Give the extent of all Trypanosoma brucei.
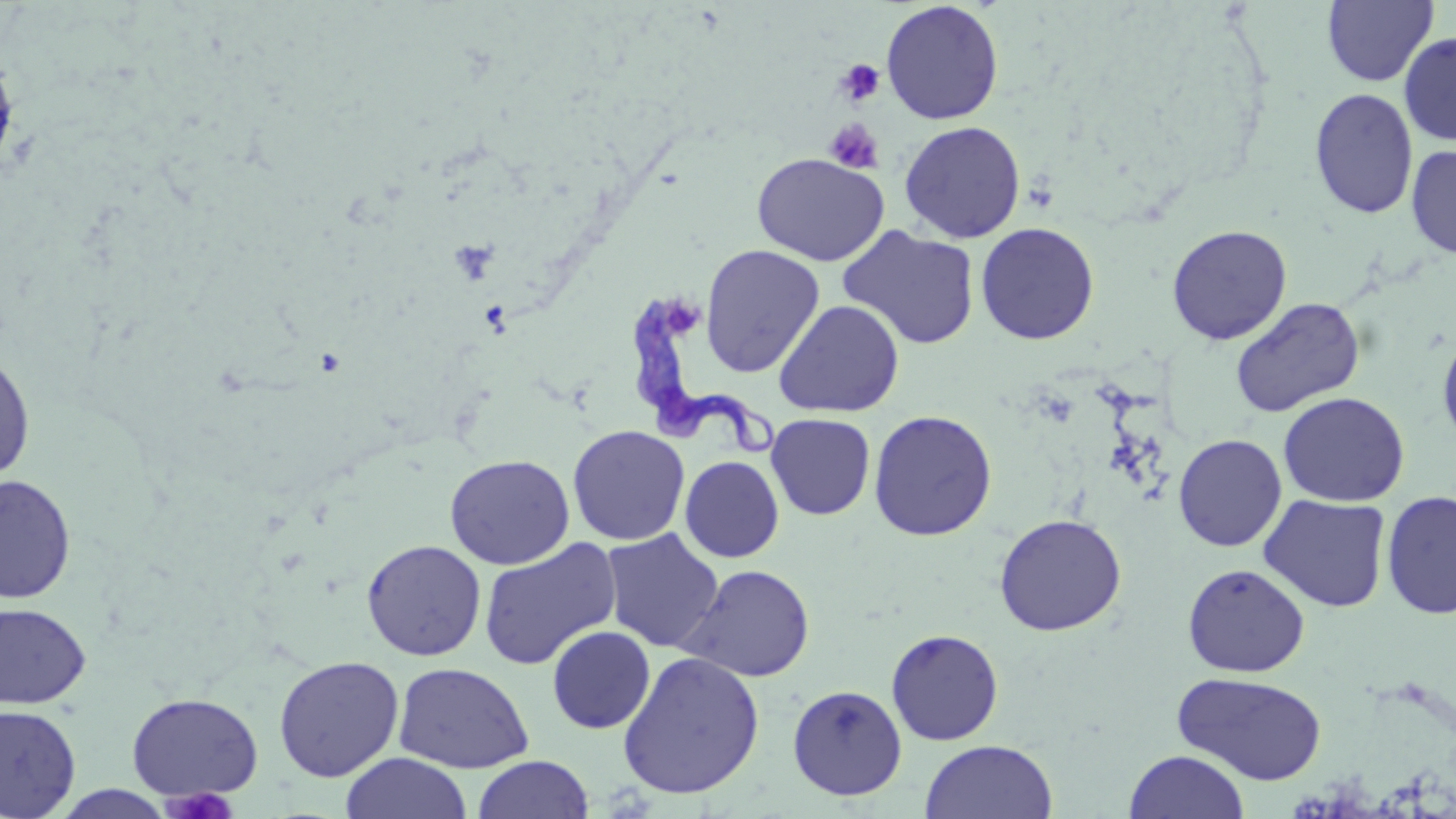
Approximate bounding boxes as (x1,y1)-(x2,y2) corner pairs in pixels.
Trypanosoma brucei: (629,289)-(778,457).

Uninfected red blood cell locations: (880,1)-(1004,125), (1321,1)-(1439,86), (1398,31)-(1456,146), (0,43)-(20,180), (1309,87)-(1419,219), (899,120)-(1026,243), (1406,144)-(1456,259), (751,152)-(889,266), (975,222)-(1100,345), (1166,224)-(1292,345), (837,225)-(981,350), (699,244)-(825,378), (1229,296)-(1365,417), (773,299)-(905,417), (1437,325)-(1456,454), (0,347)-(36,485), (1277,391)-(1410,507), (868,409)-(998,541), (766,413)-(876,520), (567,425)-(690,545), (1173,433)-(1287,551), (444,453)-(575,570), (680,456)-(785,562), (0,474)-(77,604), (1380,490)-(1456,619), (1258,494)-(1392,612), (993,513)-(1126,636), (600,528)-(724,653), (478,537)-(622,671), (361,538)-(487,661), (1182,563)-(1309,677), (679,564)-(816,683), (0,601)-(92,710), (546,625)-(655,733), (886,628)-(1004,745), (616,651)-(765,800), (273,655)-(405,782), (393,661)-(534,773), (1172,671)-(1328,785), (787,684)-(907,800), (126,692)-(263,801), (0,703)-(81,819), (919,739)-(1057,819), (1124,749)-(1249,818), (341,752)-(471,818), (472,754)-(594,818). Platelet locations: (835,58)-(886,108), (824,119)-(885,174), (159,787)-(240,818). Slide-level diagnosis: Trypanosoma brucei. One field of a larger specimen. Captured at 1000x magnification. Optical microscopy. Image is 1456×819 pixels. Thin blood film. May-Grünwald-Giemsa stain.